Locate every Plasmodium vivax-infected red blood cell.
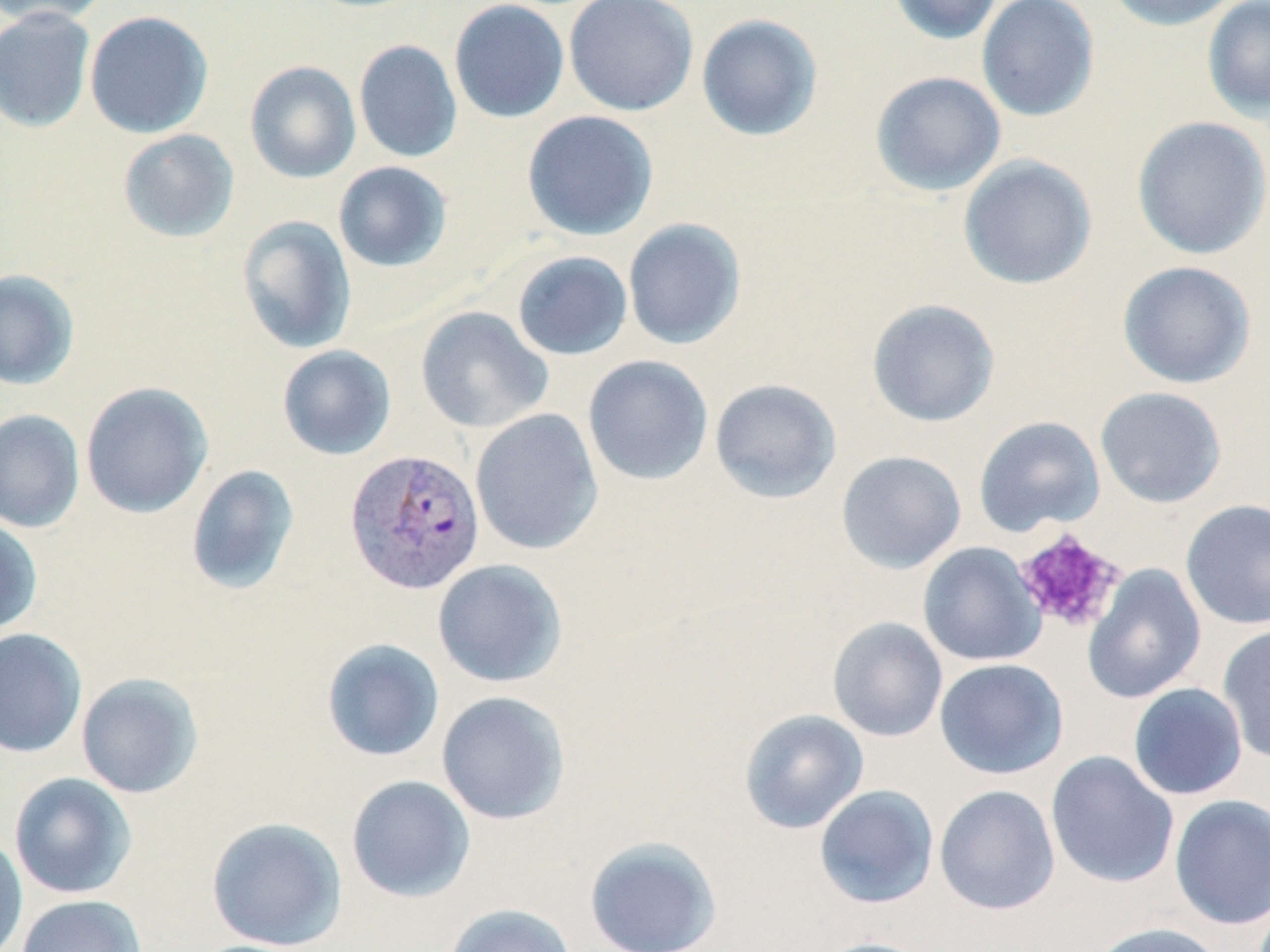

Approximate bounding boxes as (x1, y1, x2, y2) in pixels.
Plasmodium vivax-infected red blood cells: (345, 448, 485, 595).

Uninfected red blood cell locations: (0, 0, 110, 28), (449, 0, 570, 124), (564, 0, 699, 116), (887, 0, 1004, 45), (976, 0, 1100, 122), (1102, 0, 1243, 31), (1201, 0, 1270, 122), (0, 7, 96, 133), (84, 10, 214, 138), (696, 13, 824, 142), (354, 39, 462, 163), (244, 60, 361, 184), (870, 70, 1007, 197), (521, 110, 659, 241), (1131, 115, 1270, 260), (118, 129, 240, 243), (958, 154, 1098, 290), (333, 162, 452, 272), (236, 215, 357, 355), (622, 218, 747, 350), (511, 250, 633, 361), (1117, 260, 1257, 389), (0, 269, 81, 391), (866, 298, 1001, 427), (415, 306, 552, 434), (276, 345, 397, 460), (583, 355, 713, 485), (709, 378, 842, 504), (81, 382, 213, 519), (1095, 386, 1227, 508), (470, 408, 603, 555), (0, 409, 85, 533), (974, 416, 1105, 537), (836, 450, 967, 574), (185, 464, 301, 595), (1180, 498, 1270, 630), (0, 515, 43, 636), (918, 542, 1046, 667), (432, 558, 568, 688), (1082, 563, 1206, 704), (827, 616, 948, 743), (1217, 623, 1270, 763), (0, 628, 87, 758), (321, 638, 445, 762), (934, 658, 1069, 779), (76, 672, 204, 799), (1128, 683, 1248, 800), (436, 691, 571, 825), (739, 709, 869, 834), (1045, 751, 1180, 889), (9, 772, 137, 900), (346, 775, 476, 903), (813, 784, 940, 909), (934, 784, 1060, 915), (1169, 795, 1270, 930), (206, 816, 347, 952), (0, 833, 29, 952), (584, 835, 722, 952), (16, 894, 147, 952), (444, 903, 577, 952), (1089, 921, 1227, 952), (810, 937, 934, 952). Platelet locations: (1013, 528, 1127, 634). Slide-level diagnosis: Plasmodium vivax. Image is 1270×952 pixels. Thin blood smear. 1000x magnification. One field of a larger specimen. May-Grünwald-Giemsa-stained preparation. Optical microscopy.